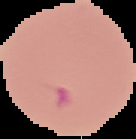 From a thin blood film. Cell region segmented out of the field of view; the surrounding area is masked to black. Image is 136×139 pixels. Result: Plasmodium parasites identified.